Look for Plasmodium parasites.
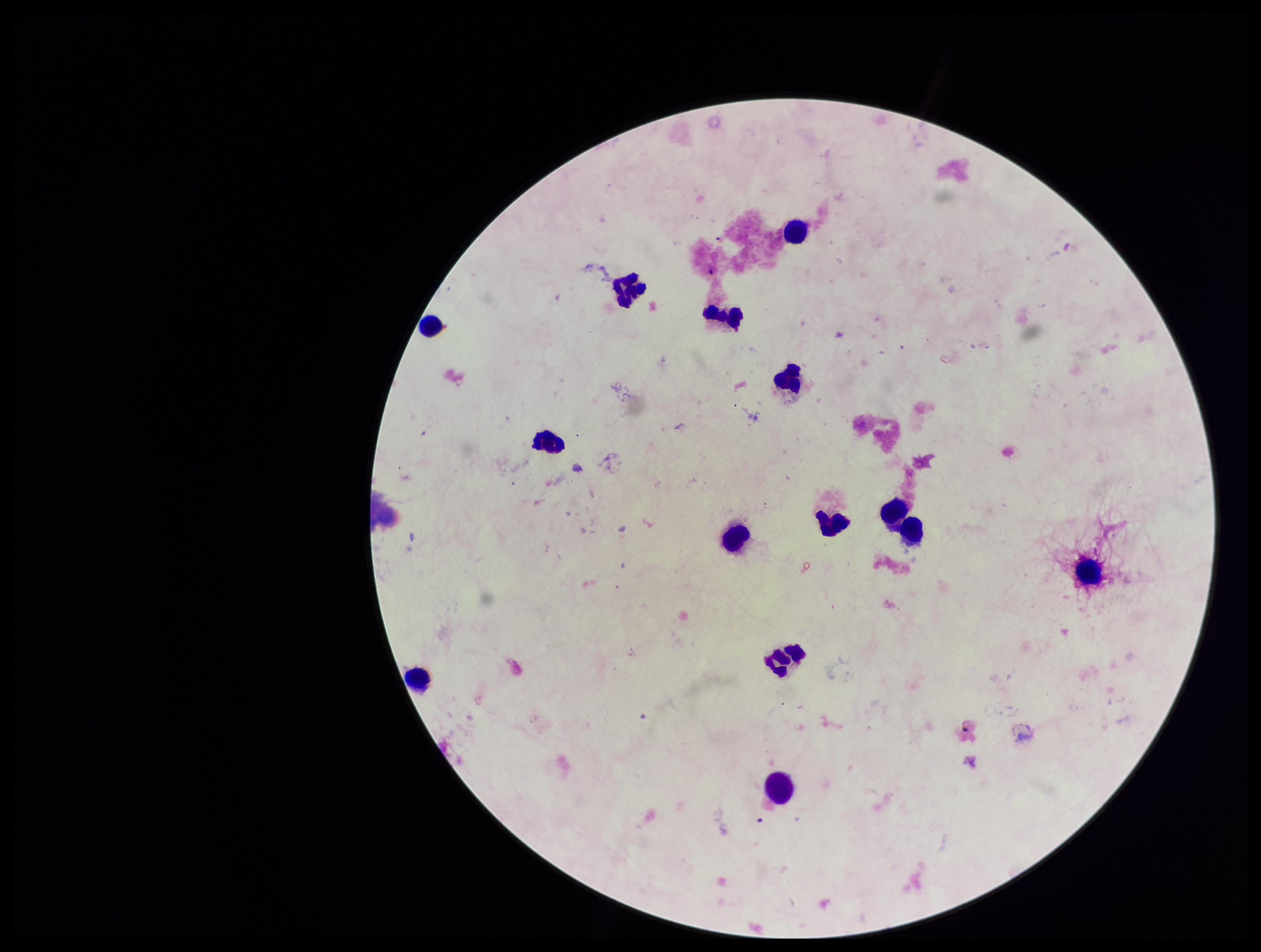

None identified.

stain = Giemsa
leukocyte count = 14
field of view = single
capture = smartphone photograph through the microscope eyepiece
parasite count = 0
preparation = thick
image size = 1261×952 pixels
patient malaria status = negative